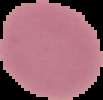
{
  "preparation": "thin blood smear",
  "image_type": "cell region segmented out of the field of view; surrounding area masked to black",
  "image_size": "103×100 pixels",
  "malaria_status": "uninfected"
}